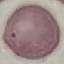

Summary:
  - Malaria status: uninfected
  - Capture: smartphone camera at the microscope eyepiece
  - Stain: Giemsa
  - Image type: automatically extracted cell patch, resized to 64 × 64 pixels
  - Preparation: thin blood smear